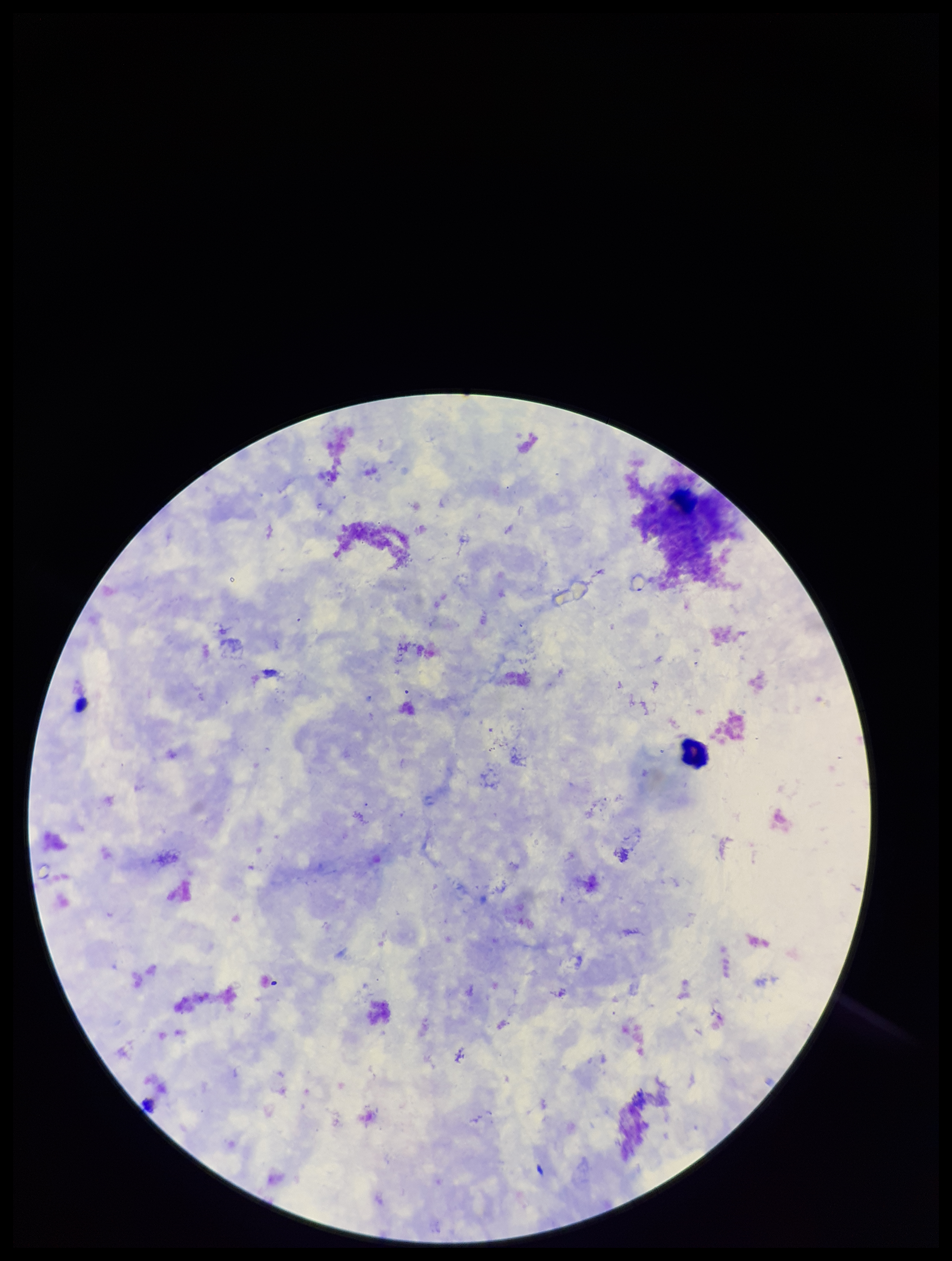

Summary:
  - Patient malaria status: negative
  - Field of view: one from this slide
  - Image size: 952×1261 pixels
  - Capture: smartphone photograph through the microscope eyepiece
  - Preparation: thick blood smear
  - Stain: Giemsa
  - Plasmodium parasites: none detected
  - Leukocyte count: 1
  - Parasite count: 0